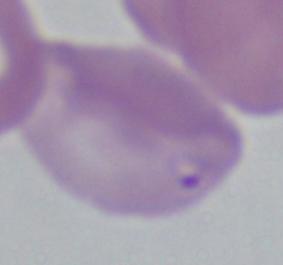

Micrograph. A Babesia parasite is seen. 1000x magnification.